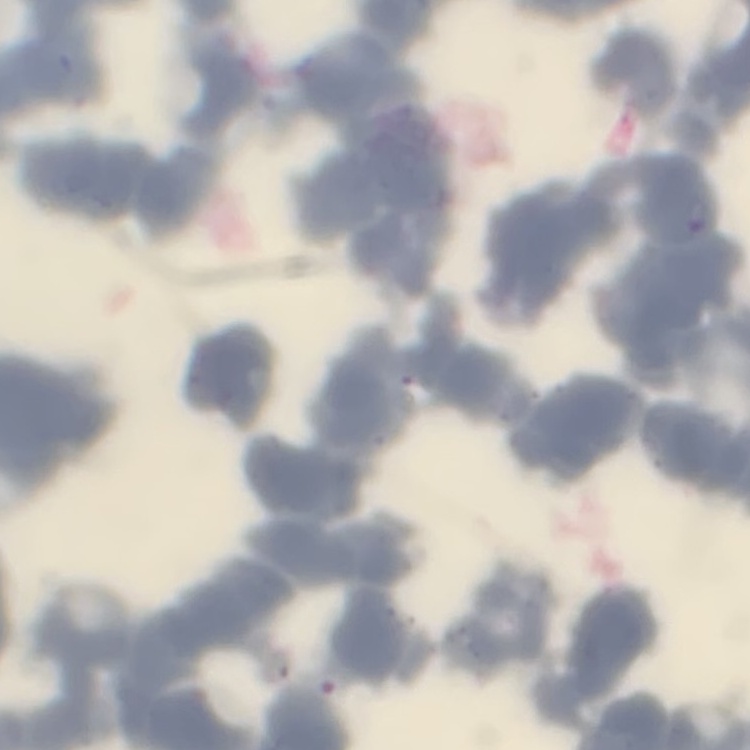
Summary:
  - Erythrocyte morphology: rouleaux formation
  - Stain: Field's or Giemsa
  - Preparation: thin blood film
  - Image type: square crop of a larger photomicrograph